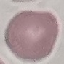
Result: no malaria parasites seen. Photographed with a smartphone camera at the microscope eyepiece. Thin smear of blood. Giemsa-stained preparation. Automatically extracted cell patch, resized to 64 × 64 pixels.